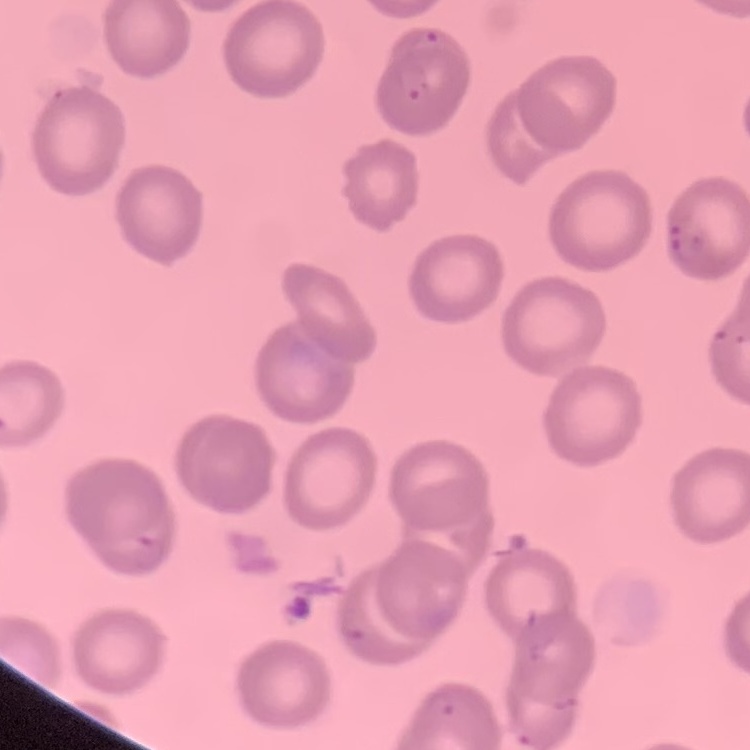

The erythrocytes exhibit no rouleaux formation. Thin peripheral smear. One tile cut from a larger photomicrograph. Field's or Giemsa stain.